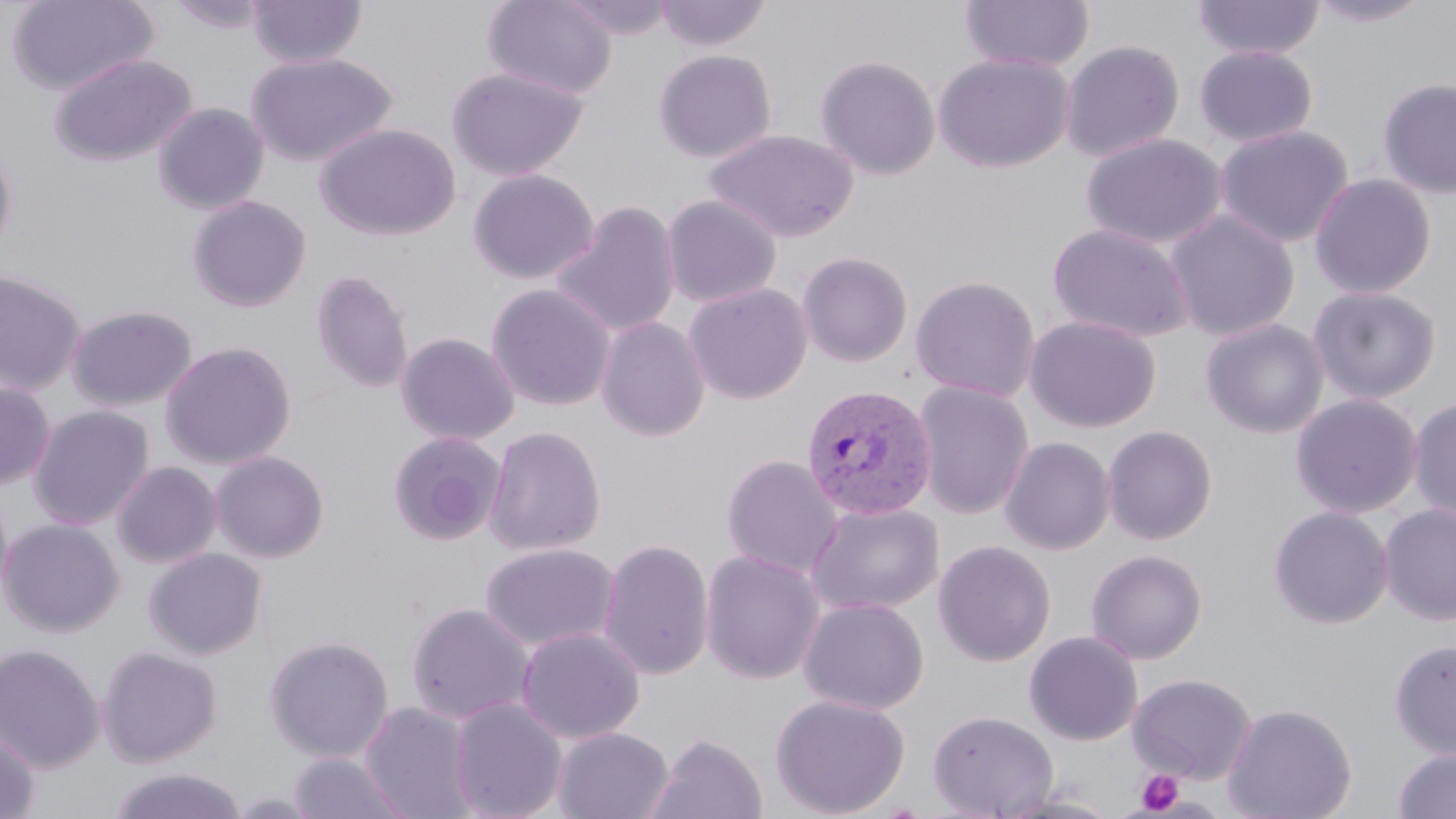
slide-level diagnosis = Plasmodium vivax
image size = 1456×819 pixels
modality = light microscopy
magnification = 1000x
stain = May-Grünwald-Giemsa
uninfected red blood cell locations = approximate bounding boxes as (x1,y1)-(x2,y2) corner pairs in pixels: (7,0)-(158,97), (166,0)-(272,33), (247,0)-(367,68), (482,0)-(617,100), (557,0)-(677,39), (655,0)-(770,51), (1191,0)-(1326,61), (1306,0)-(1433,27), (959,1)-(1094,73), (1060,40)-(1185,162), (1194,45)-(1318,148), (653,49)-(777,163), (245,52)-(398,167), (49,53)-(197,168), (933,53)-(1074,173), (814,55)-(941,180), (446,67)-(589,181), (1377,77)-(1456,199), (152,102)-(270,215), (316,123)-(461,241), (1215,124)-(1354,248), (704,128)-(859,243), (1080,132)-(1228,251), (0,138)-(17,257), (170,139)-(309,266), (468,168)-(599,285), (1309,173)-(1437,300), (661,194)-(782,308), (187,195)-(312,312), (551,201)-(682,338), (1164,209)-(1300,342), (1047,222)-(1195,343), (797,251)-(913,367), (0,269)-(87,395), (311,270)-(414,393), (910,275)-(1041,402), (683,282)-(813,404), (486,283)-(616,411), (1307,286)-(1442,404), (66,304)-(198,412), (1024,315)-(1160,433), (595,316)-(710,442), (1200,318)-(1328,439), (395,331)-(520,446), (160,340)-(297,470), (0,381)-(56,490), (912,381)-(1034,519), (1290,393)-(1422,518), (1408,397)-(1456,522), (28,405)-(154,530), (484,425)-(606,556), (1102,425)-(1218,545), (387,431)-(507,546), (999,436)-(1116,555), (210,451)-(329,562), (721,455)-(843,579), (111,461)-(221,568), (0,481)-(14,605), (805,501)-(945,616), (1378,503)-(1456,626), (1269,505)-(1393,629), (0,517)-(124,637), (599,537)-(715,681), (933,540)-(1056,666), (479,542)-(621,653), (144,547)-(267,660), (1086,548)-(1207,665), (700,549)-(826,685), (798,596)-(930,715), (405,602)-(534,726), (516,626)-(645,744), (1024,631)-(1143,745), (264,634)-(394,762), (1388,639)-(1456,760), (0,643)-(105,772), (97,646)-(222,766), (1128,673)-(1256,784), (769,693)-(910,817), (449,697)-(567,819), (359,701)-(478,819), (1222,702)-(1357,819), (928,709)-(1058,818), (552,727)-(674,819), (0,729)-(39,819), (644,733)-(768,819), (1392,747)-(1456,818), (286,751)-(412,819), (107,767)-(249,819), (992,790)-(1122,819)
preparation = thin blood smear
Plasmodium vivax-infected red blood cell locations = approximate bounding boxes as (x1,y1)-(x2,y2) corner pairs in pixels: (801,383)-(938,521)
field of view = single
platelet locations = approximate bounding boxes as (x1,y1)-(x2,y2) corner pairs in pixels: (1134,769)-(1184,815)